Locate every Plasmodium parasite.
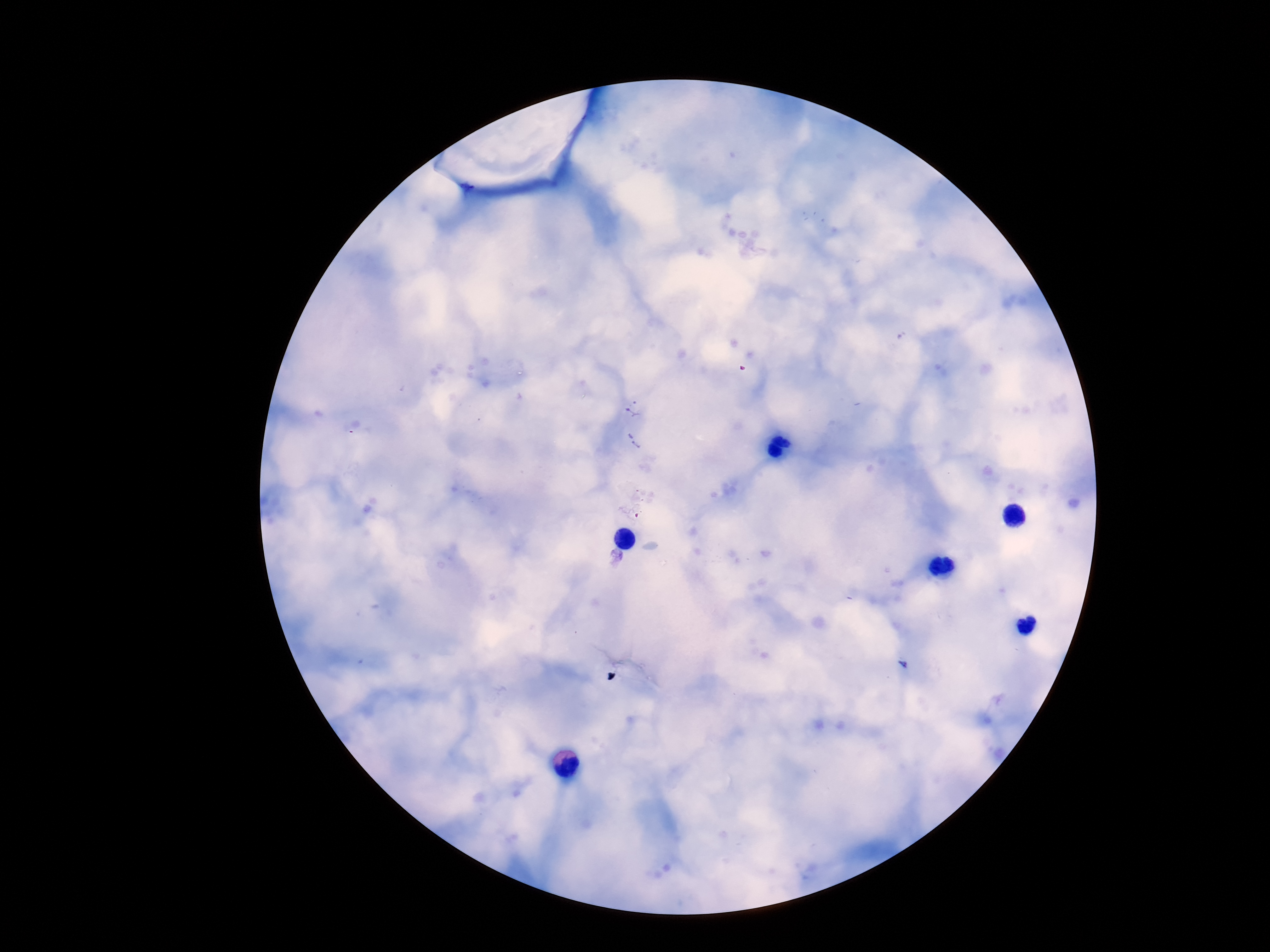
Approximate object centers, in pixels from the top-left corner.
Plasmodium parasites: (x=634, y=408), (x=632, y=440), (x=615, y=558).

{
  "stain": "Giemsa",
  "capture": "smartphone camera through the microscope eyepiece",
  "image_size": "1270×952 pixels",
  "preparation": "thick blood film",
  "field_of_view": "single",
  "patient_malaria_status": "positive",
  "magnification": "100x"
}